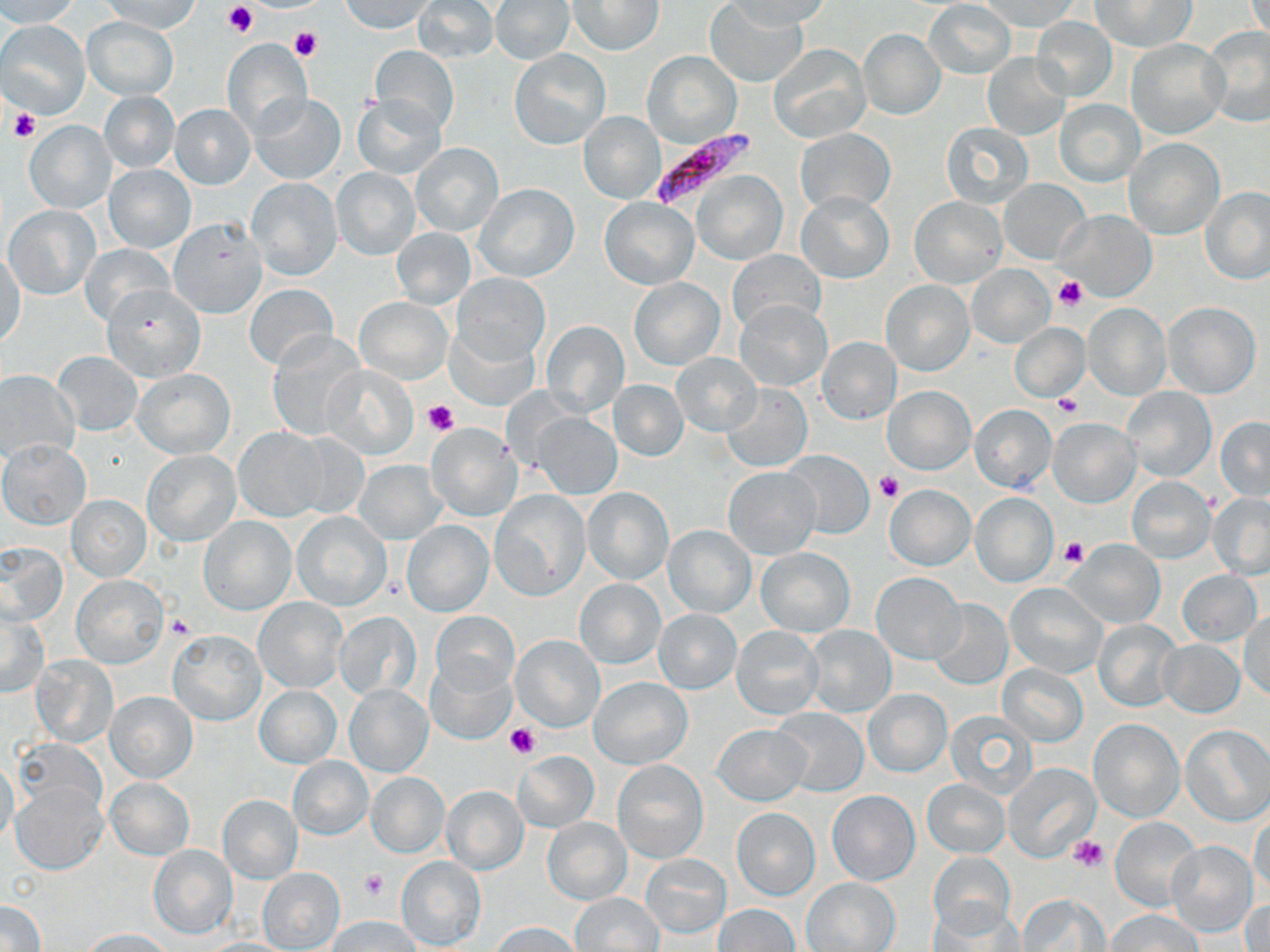

Approximate bounding boxes as [x1, y1, x2, y2] in pixels. Plasmodium falciparum-infected red blood cell locations: [648, 129, 760, 207]. Uninfected red blood cell locations: [0, 0, 82, 28], [99, 0, 201, 32], [340, 0, 433, 34], [414, 0, 498, 63], [724, 0, 828, 33], [1245, 0, 1268, 47], [490, 1, 575, 64], [568, 1, 664, 55], [978, 1, 1082, 32], [1092, 1, 1196, 52], [705, 2, 807, 87], [923, 2, 1015, 79], [82, 16, 179, 99], [1032, 19, 1116, 100], [0, 20, 92, 117], [1201, 26, 1270, 127], [858, 28, 945, 120], [222, 38, 312, 138], [1126, 39, 1229, 141], [769, 44, 870, 142], [370, 46, 458, 135], [510, 49, 610, 149], [642, 51, 741, 148], [982, 52, 1070, 140], [99, 91, 180, 173], [248, 92, 346, 185], [353, 94, 446, 181], [1054, 100, 1144, 186], [169, 104, 255, 189], [579, 113, 664, 202], [24, 120, 116, 214], [941, 120, 1035, 211], [796, 129, 895, 214], [1123, 137, 1224, 238], [410, 144, 503, 236], [104, 164, 194, 253], [331, 167, 419, 261], [694, 171, 786, 264], [247, 177, 342, 281], [998, 178, 1091, 264], [475, 183, 580, 283], [1201, 186, 1270, 284], [797, 192, 893, 283], [598, 196, 698, 289], [909, 196, 1006, 288], [4, 206, 101, 299], [1053, 209, 1157, 302], [167, 217, 266, 318], [391, 227, 475, 309], [79, 245, 177, 325], [1, 251, 25, 350], [727, 251, 825, 333], [966, 264, 1055, 349], [453, 274, 550, 367], [627, 276, 725, 370], [880, 279, 974, 376], [244, 284, 338, 372], [102, 285, 205, 382], [355, 296, 452, 383], [736, 301, 830, 391], [1163, 302, 1261, 398], [1084, 303, 1170, 400], [542, 319, 630, 413], [1011, 323, 1088, 403], [266, 331, 368, 441], [817, 337, 901, 423], [53, 351, 143, 436], [672, 352, 761, 436], [324, 365, 418, 459], [0, 369, 80, 461], [132, 369, 236, 459], [609, 379, 688, 460], [723, 382, 811, 471], [882, 386, 975, 474], [1121, 386, 1216, 482], [969, 404, 1057, 494], [533, 413, 622, 499], [1216, 416, 1270, 502], [1049, 418, 1141, 507], [425, 422, 521, 523], [233, 428, 327, 522], [287, 431, 369, 519], [0, 439, 92, 530], [142, 449, 241, 546], [786, 450, 875, 538], [354, 460, 445, 544], [724, 466, 820, 559], [1127, 477, 1215, 563], [885, 485, 975, 570], [583, 488, 673, 585], [489, 490, 590, 601], [970, 493, 1058, 586], [1208, 494, 1270, 579], [67, 495, 150, 580], [291, 511, 391, 611], [199, 516, 295, 614], [402, 520, 494, 617], [663, 526, 755, 616], [1065, 539, 1165, 627], [0, 542, 66, 627], [755, 546, 854, 636], [1178, 569, 1262, 645], [871, 573, 964, 663], [71, 575, 168, 668], [575, 579, 664, 668], [1005, 582, 1106, 678], [253, 596, 348, 693], [927, 598, 1013, 690], [2, 607, 50, 697], [654, 609, 741, 693], [334, 611, 421, 700], [431, 612, 518, 695], [1240, 612, 1270, 701], [1093, 620, 1180, 711], [731, 625, 825, 719], [803, 625, 897, 717], [168, 629, 265, 725], [511, 636, 604, 731], [1159, 640, 1244, 717], [31, 656, 118, 747], [426, 660, 516, 743], [999, 663, 1087, 745], [590, 676, 692, 769], [342, 684, 434, 776], [255, 685, 341, 767], [863, 689, 951, 776], [106, 691, 197, 783], [771, 708, 869, 795], [946, 709, 1039, 799], [1089, 719, 1182, 822], [713, 723, 811, 805], [1181, 724, 1269, 825], [13, 739, 106, 822], [513, 751, 598, 832], [288, 756, 373, 839], [0, 757, 20, 848], [612, 759, 709, 864], [1004, 763, 1100, 861], [366, 772, 448, 857], [105, 777, 193, 860], [923, 780, 1008, 857], [11, 782, 108, 875], [443, 785, 528, 874], [828, 790, 920, 885], [217, 794, 302, 883], [732, 809, 819, 899], [1250, 811, 1270, 900], [1110, 816, 1203, 911], [543, 817, 631, 904], [1165, 841, 1258, 937], [148, 844, 238, 939], [930, 851, 1016, 937], [640, 853, 731, 937], [395, 856, 485, 950], [257, 866, 346, 951], [802, 877, 900, 951], [571, 892, 663, 952], [1242, 893, 1269, 951], [1018, 894, 1106, 950], [0, 899, 45, 952], [715, 903, 799, 951], [929, 905, 1023, 952], [1107, 909, 1202, 952], [327, 916, 422, 951], [491, 922, 581, 952], [79, 928, 172, 951]. Platelet locations: [221, 2, 257, 38], [288, 26, 321, 61], [10, 108, 39, 140], [1053, 275, 1088, 311], [1053, 393, 1082, 417], [422, 399, 459, 435], [874, 473, 902, 502], [1061, 537, 1089, 567], [167, 614, 195, 639], [504, 724, 539, 758], [1069, 835, 1105, 872], [360, 869, 389, 900]. Slide-level diagnosis: Plasmodium falciparum. Single field of view. May-Grünwald-Giemsa-stained preparation. Thin blood film. Image is 1270×952 pixels. Light microscopy. Captured at 1000x magnification.